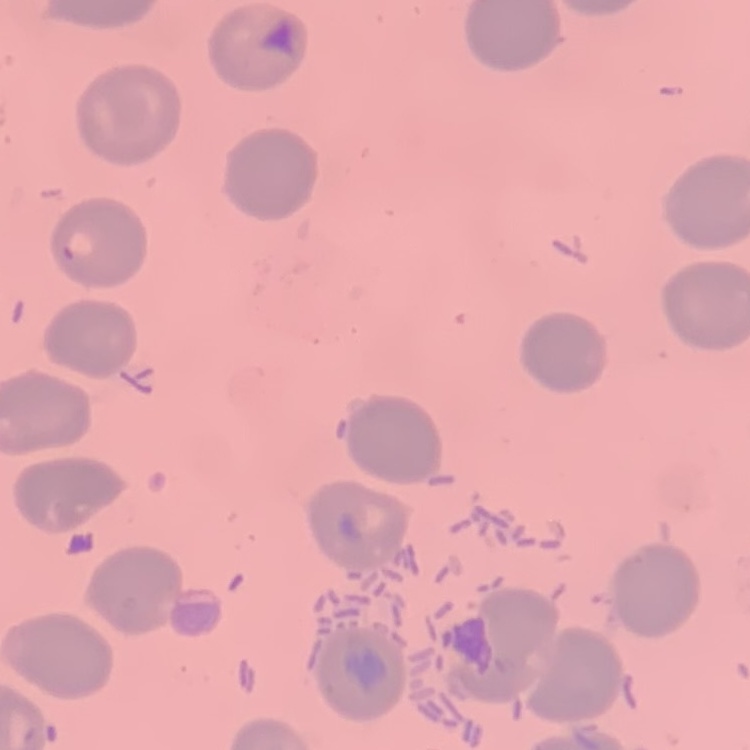 The red blood cells exhibit no rouleaux formation. Stained with either Field's or Giemsa. Thin peripheral smear. One tile cut from a larger photomicrograph.